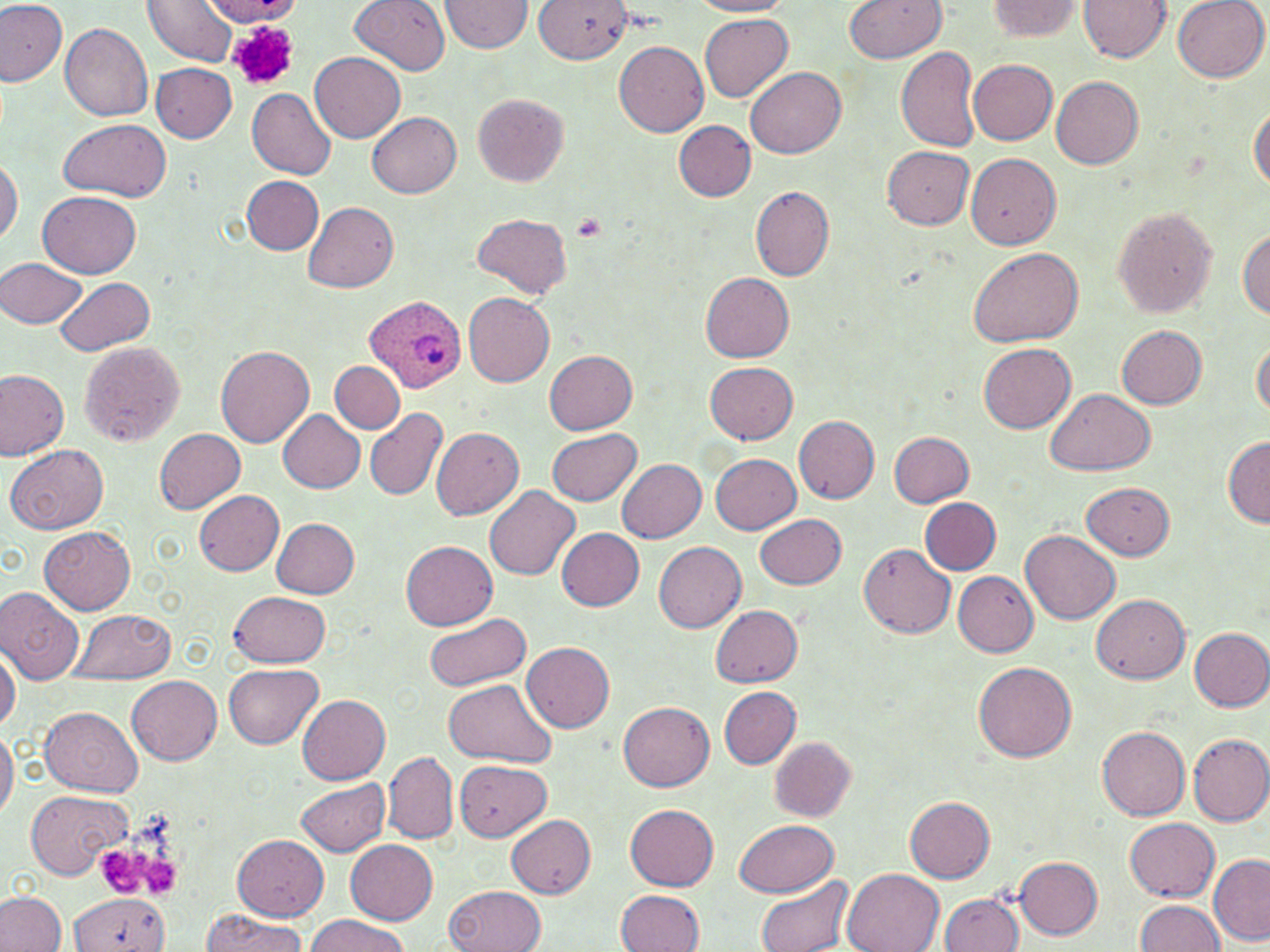

Approximate bounding boxes as [x1, y1, x2, y2] in pixels. Platelet locations: [228, 20, 298, 91], [572, 213, 607, 241], [97, 847, 146, 893], [134, 849, 183, 899]. Plasmodium ovale-infected red blood cell locations: [364, 293, 466, 394]. Uninfected red blood cell locations: [0, 0, 68, 87], [143, 0, 239, 66], [351, 0, 452, 74], [438, 0, 533, 53], [532, 0, 633, 64], [690, 0, 794, 16], [843, 0, 949, 63], [1079, 0, 1171, 63], [1172, 0, 1268, 83], [203, 1, 301, 24], [984, 1, 1087, 41], [699, 13, 794, 102], [60, 21, 154, 121], [614, 41, 709, 136], [896, 47, 981, 153], [310, 53, 405, 143], [968, 58, 1058, 144], [150, 63, 237, 142], [746, 66, 846, 158], [1051, 76, 1145, 169], [247, 89, 337, 179], [472, 93, 568, 185], [1249, 104, 1270, 193], [367, 112, 462, 198], [59, 118, 170, 200], [673, 121, 755, 200], [883, 145, 975, 228], [966, 153, 1061, 248], [0, 156, 23, 246], [242, 176, 322, 255], [750, 185, 835, 281], [38, 189, 142, 277], [303, 202, 400, 294], [1111, 206, 1219, 318], [471, 213, 572, 297], [1237, 227, 1270, 320], [966, 244, 1083, 346], [1, 256, 88, 328], [700, 273, 794, 362], [54, 276, 155, 353], [464, 293, 555, 387], [1117, 326, 1207, 409], [77, 340, 186, 447], [1252, 340, 1269, 419], [979, 343, 1075, 433], [216, 344, 313, 447], [545, 349, 638, 434], [336, 360, 424, 482], [331, 361, 404, 433], [705, 361, 798, 444], [0, 369, 69, 460], [1, 374, 84, 532], [1046, 389, 1156, 476], [366, 408, 449, 501], [278, 410, 365, 493], [793, 414, 880, 504], [430, 427, 524, 519], [547, 427, 641, 506], [153, 428, 246, 514], [889, 431, 974, 507], [1222, 437, 1270, 526], [7, 443, 108, 533], [711, 453, 800, 533], [617, 460, 706, 543], [1083, 481, 1175, 559], [485, 485, 579, 580], [194, 490, 284, 575], [919, 496, 1001, 574], [755, 512, 847, 590], [271, 518, 360, 598], [40, 525, 136, 614], [556, 528, 645, 609], [1022, 530, 1120, 624], [401, 539, 498, 630], [654, 541, 747, 632], [858, 542, 957, 639], [953, 571, 1038, 657], [0, 586, 85, 685], [229, 591, 330, 667], [1089, 593, 1190, 682], [711, 604, 803, 687], [74, 608, 173, 682], [423, 611, 531, 691], [1189, 627, 1270, 710], [0, 641, 19, 734], [522, 641, 615, 733], [974, 659, 1076, 761], [225, 664, 323, 748], [127, 675, 222, 764], [442, 679, 555, 766], [719, 686, 801, 768], [298, 695, 389, 782], [620, 702, 714, 791], [41, 706, 143, 797], [1097, 726, 1191, 820], [0, 727, 17, 821], [1187, 734, 1270, 826], [769, 737, 856, 820], [384, 752, 457, 844], [455, 760, 551, 841], [296, 777, 389, 857], [27, 790, 132, 880], [905, 795, 995, 882], [625, 804, 719, 891], [507, 814, 596, 897], [1125, 818, 1220, 901], [732, 820, 840, 896], [233, 834, 328, 922], [346, 840, 438, 924], [1208, 853, 1270, 944], [1013, 856, 1102, 938], [843, 869, 944, 952], [755, 873, 852, 952], [445, 885, 545, 952], [614, 890, 704, 952], [0, 891, 67, 952], [940, 892, 1024, 951], [68, 893, 169, 952], [1135, 899, 1226, 951], [201, 910, 309, 952], [307, 915, 408, 952]. Slide-level diagnosis: Plasmodium ovale. Image is 1270×952 pixels. Captured at 1000x magnification. May-Grünwald-Giemsa stain. Single field of view. Optical microscopy. Thin blood film.